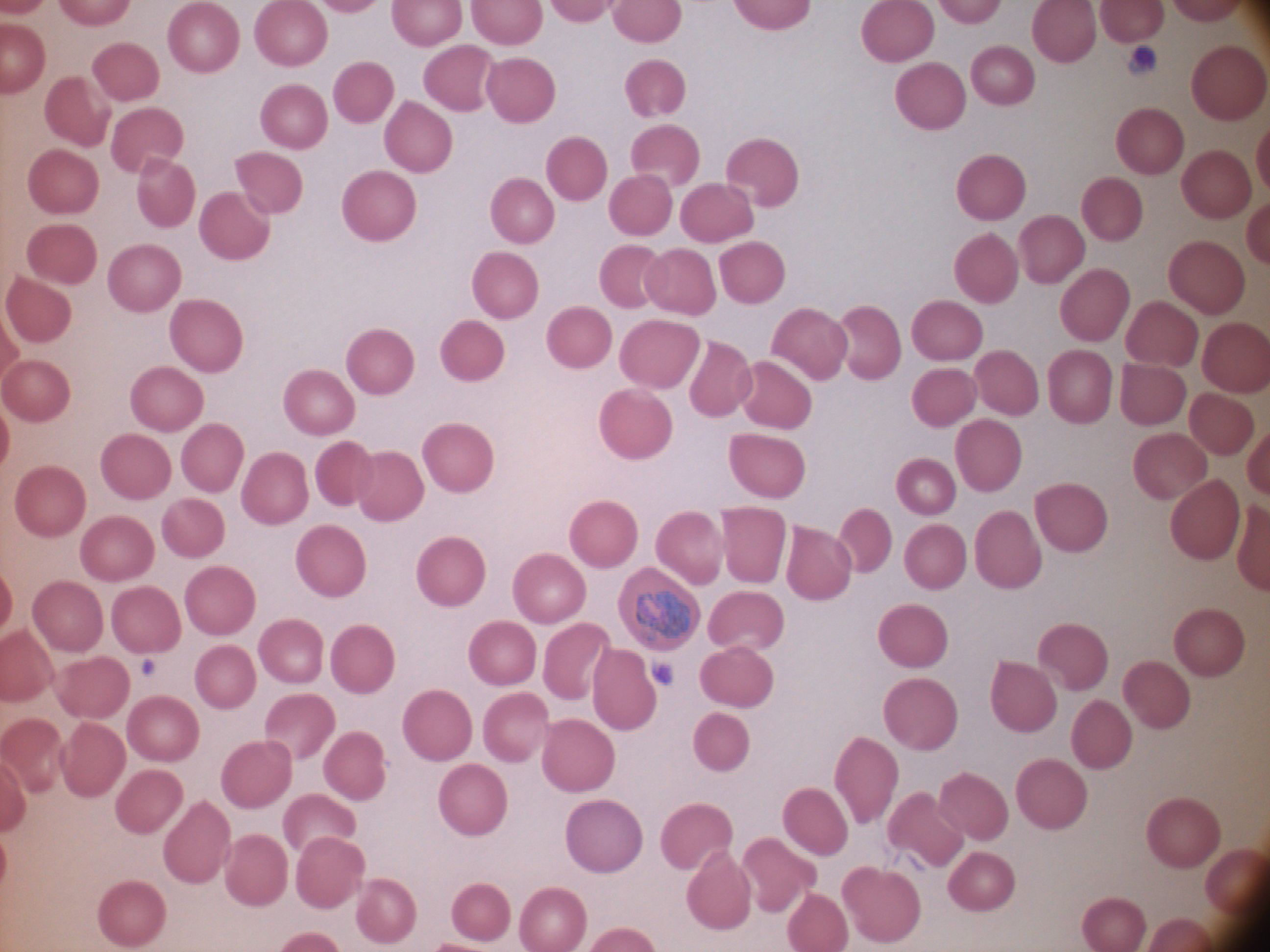
trophozoite locations = approximate bounding boxes as named x1/y1/x2/y2 corners in pixels, from the source annotation, which is not necessarily exhaustive: (x1=633, y1=589, x2=690, y2=644)
preparation = thin blood film
image size = 1270×952 pixels
field of view = single
stain = Giemsa
magnification = 100x
microscope = Leica DM2000 with built-in camera
species = Plasmodium ovale